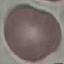 Result: no malaria parasites detected. Giemsa stain. Thin blood film. Cell patch, automatically extracted from a larger field of view and resized to 64 × 64 pixels. Photographed with a smartphone camera at the microscope eyepiece.